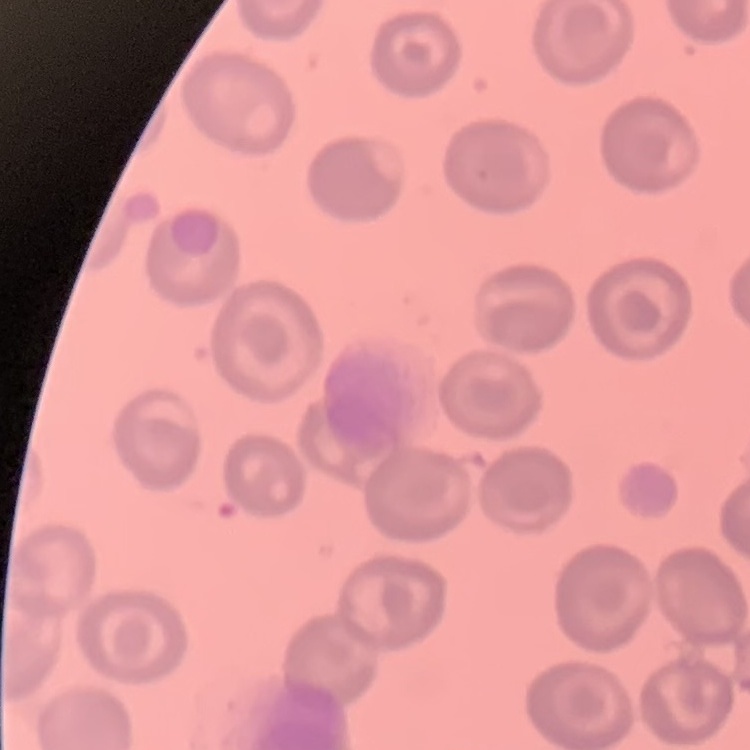

Summary:
  - Red blood cell morphology: no rouleaux formation
  - Stain: Field's or Giemsa
  - Preparation: thin peripheral smear
  - Image type: square crop of a larger photomicrograph